Identify the parasite.
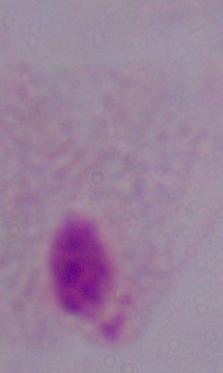
This is a trichomonad.

Summary:
  - Modality: micrograph
  - Magnification: 1000x